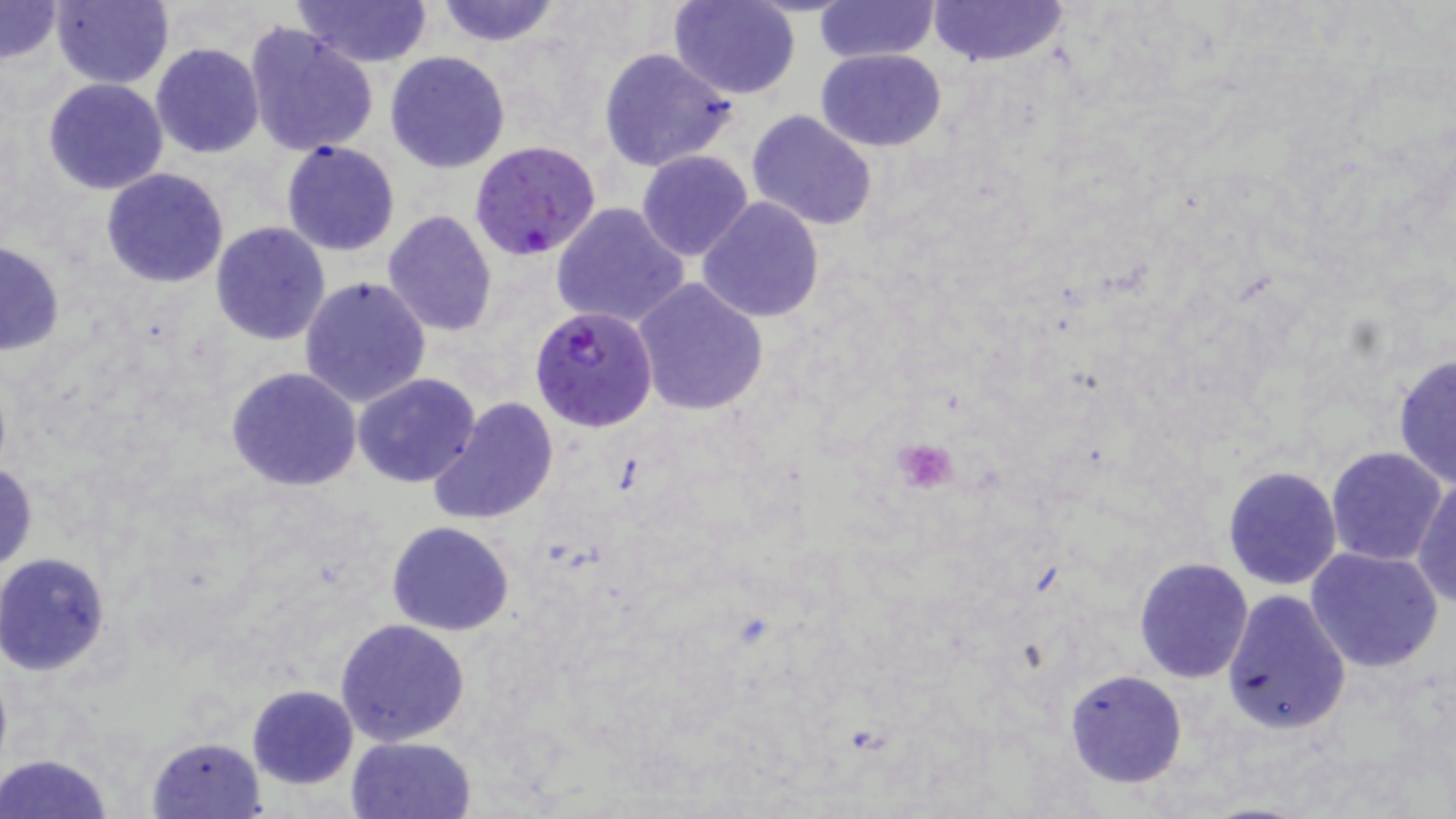
Approximate bounding boxes as (x1,y1)-(x2,y2) corner pairs in pixels. Uninfected red blood cell locations: (0,0)-(64,65), (52,0)-(173,88), (293,0)-(432,67), (433,0)-(560,47), (670,0)-(801,99), (927,0)-(1068,67), (813,1)-(943,62), (243,22)-(377,158), (151,43)-(264,159), (599,47)-(736,171), (815,48)-(947,151), (385,51)-(510,173), (42,78)-(169,195), (746,109)-(877,230), (280,140)-(400,256), (637,149)-(753,262), (652,158)-(806,306), (100,167)-(229,288), (697,196)-(824,323), (550,199)-(692,328), (383,209)-(499,338), (211,221)-(332,345), (0,243)-(64,354), (298,276)-(432,410), (632,277)-(769,417), (1392,353)-(1455,488), (226,367)-(361,490), (353,373)-(481,488), (428,398)-(558,526), (1326,446)-(1447,566), (1,461)-(37,572), (1222,465)-(1342,590), (1411,475)-(1456,607), (387,521)-(515,636), (1305,545)-(1445,673), (1,553)-(115,676), (1132,557)-(1254,682), (1222,590)-(1350,735), (335,618)-(470,746), (1063,669)-(1187,789), (247,684)-(359,789), (147,735)-(266,817), (345,736)-(478,819), (1,754)-(116,819). Plasmodium falciparum-infected red blood cell locations: (469,140)-(601,259), (530,305)-(657,430). Platelet locations: (893,436)-(959,493). Slide-level diagnosis: Plasmodium falciparum. Captured at 1000x magnification. One field of a larger specimen. Image is 1456×819 pixels. Thin blood film. May-Grünwald-Giemsa stain. Light microscopy.